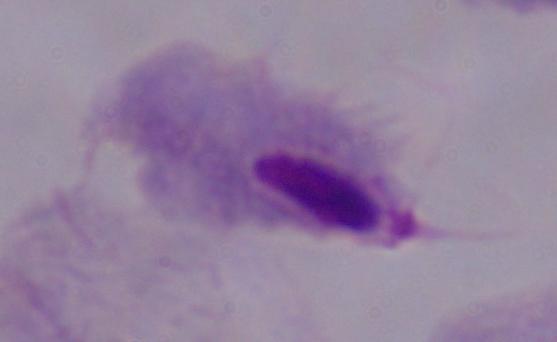

magnification = 1000x
modality = photomicrograph
identification = trichomonad